Name the cell type shown.
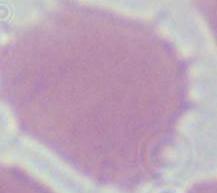

This is an erythrocyte.

modality = photomicrograph
magnification = 1000x